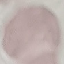

Malaria status: uninfected. Automatically extracted cell patch, resized to 64 × 64 pixels. Thin blood smear. Photographed with a smartphone camera at the microscope eyepiece. Giemsa-stained preparation.